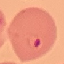 Result: malaria parasites identified. Cell patch, automatically extracted from a larger field of view and resized to 64 × 64 pixels. Acquired by smartphone through the microscope eyepiece. Giemsa-stained preparation. Thin smear of blood.